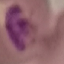

{
  "result": "malaria parasites identified",
  "capture": "smartphone camera at the microscope eyepiece",
  "stain": "Giemsa",
  "preparation": "thin smear",
  "image_type": "automatically extracted cell patch, resized to 64 × 64 pixels"
}